Classify this cell by malaria status.
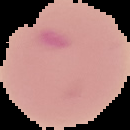

Parasitized.

Summary:
  - Preparation: thin blood smear
  - Image type: cell region segmented out of the field of view; surrounding area masked to black
  - Image size: 130×130 pixels